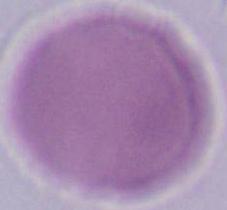
Photomicrograph. Captured at 1000x magnification. A red blood cell is seen.